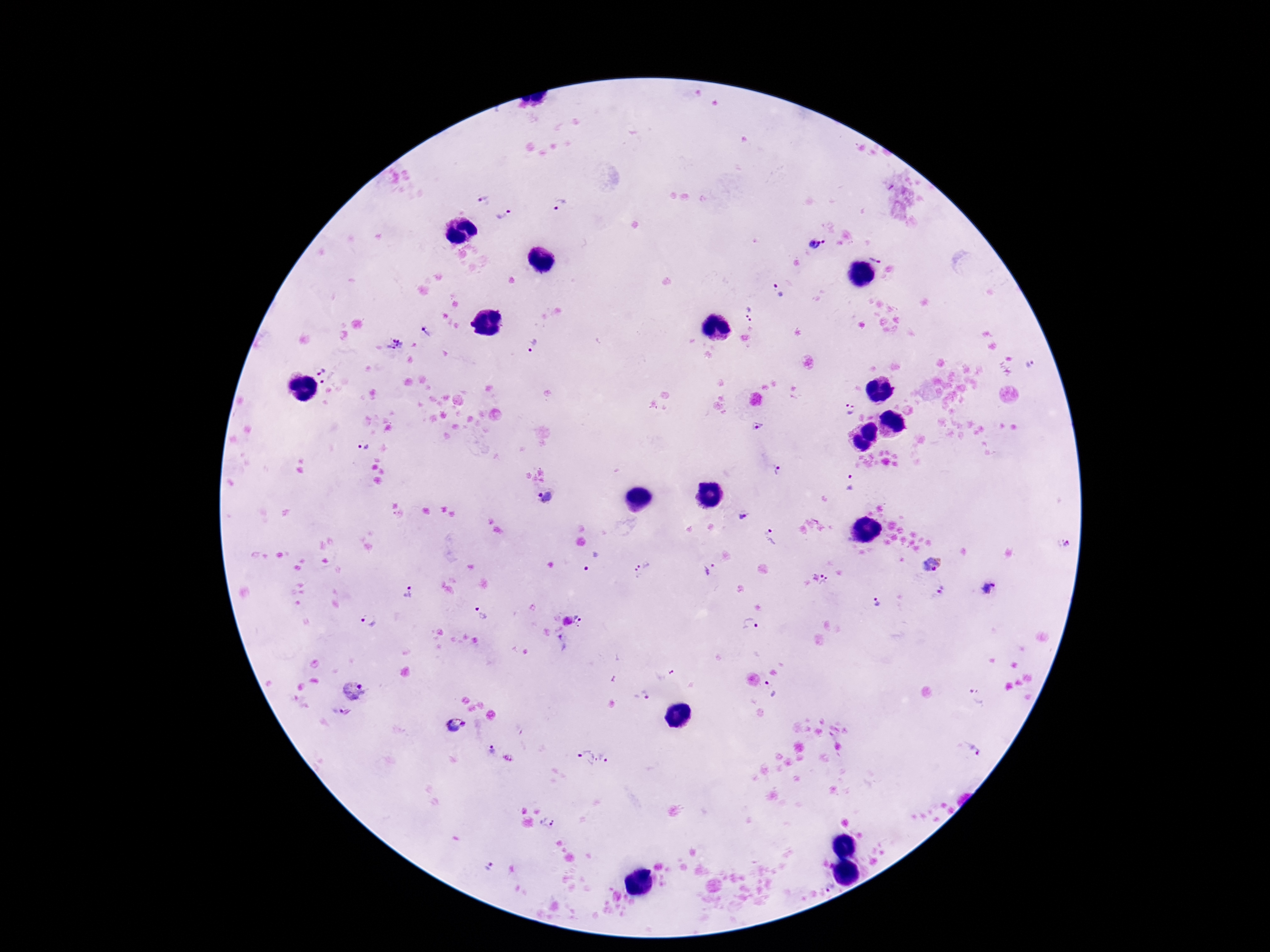
patient_malaria_status: positive
plasmodium_parasite_locations: 'approximate centers as [x, y] in pixels: [484, 200], [560, 206], [502, 214], [814, 246], [877, 253], [780, 290], [749, 313], [426, 332], [533, 344], [395, 345], [1029, 363], [318, 370], [327, 378], [850, 409], [758, 427], [364, 448], [779, 471], [849, 482], [545, 498], [742, 516], [772, 537], [1067, 544], [590, 561], [932, 564], [642, 568], [707, 571], [825, 582], [987, 587], [941, 590], [408, 593], [877, 603], [480, 612], [582, 617], [368, 620], [751, 623], [562, 642], [769, 687], [352, 692], [646, 694], [977, 695], [337, 710], [455, 727], [970, 750], [493, 751], [607, 759], [586, 760], [548, 822], [488, 864], [829, 888]'
stain: Giemsa
image_size: 1270×952 pixels
field_of_view: single
preparation: thick blood film
capture: smartphone camera through the microscope eyepiece
magnification: 100x